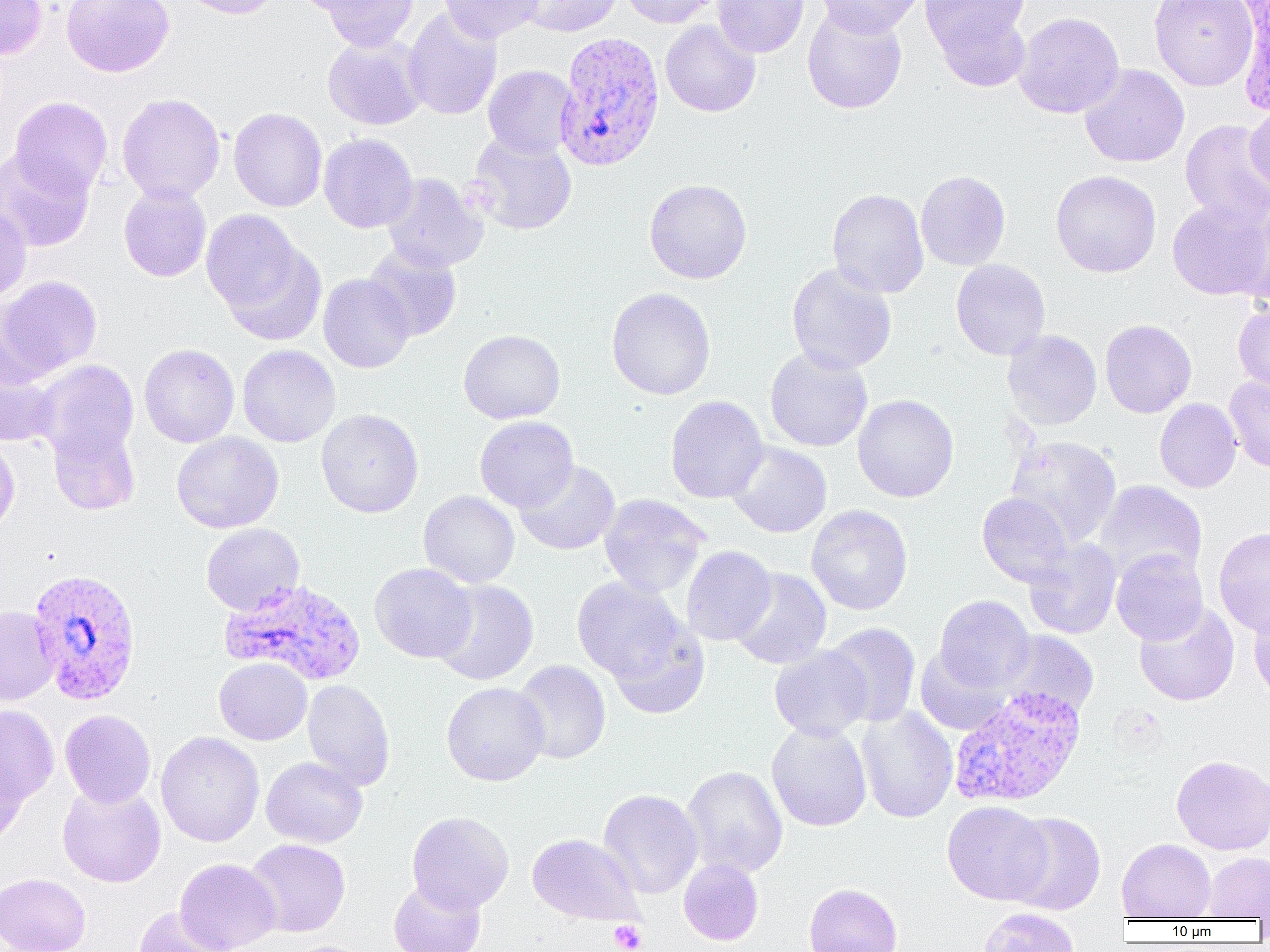

Approximate bounding boxes as (x1, y1, x2, y2) in pixels. Uninfected red blood cell locations: (0, 0, 47, 60), (60, 0, 175, 77), (177, 0, 284, 19), (287, 0, 398, 16), (316, 0, 419, 51), (438, 0, 545, 43), (515, 0, 623, 36), (620, 0, 725, 28), (713, 0, 809, 58), (815, 0, 925, 38), (921, 0, 1032, 80), (1149, 0, 1258, 91), (802, 4, 907, 114), (402, 7, 502, 121), (1013, 11, 1125, 118), (660, 20, 761, 117), (323, 34, 426, 130), (1079, 63, 1190, 168), (483, 65, 577, 159), (117, 93, 225, 204), (10, 96, 112, 199), (1245, 102, 1270, 193), (228, 107, 327, 212), (1180, 119, 1270, 227), (467, 132, 578, 235), (319, 133, 418, 233), (0, 148, 95, 252), (915, 170, 1011, 271), (1051, 170, 1162, 278), (381, 173, 488, 272), (644, 179, 752, 284), (119, 183, 211, 282), (827, 188, 929, 298), (1167, 198, 1270, 300), (0, 202, 32, 304), (1234, 202, 1270, 304), (201, 210, 308, 320), (220, 240, 327, 346), (363, 244, 462, 341), (951, 259, 1051, 360), (786, 263, 897, 374), (318, 274, 415, 373), (0, 275, 102, 380), (606, 287, 716, 400), (1233, 301, 1270, 397), (1100, 319, 1197, 418), (458, 329, 566, 424), (1002, 330, 1102, 430), (138, 344, 240, 448), (237, 345, 340, 448), (764, 346, 873, 452), (0, 354, 59, 448), (35, 359, 139, 463), (1224, 375, 1270, 473), (853, 394, 959, 502), (665, 395, 768, 503), (1155, 398, 1242, 493), (316, 408, 423, 517), (475, 416, 579, 512), (48, 421, 141, 515), (171, 431, 284, 534), (1005, 434, 1122, 548), (0, 436, 20, 539), (726, 441, 832, 538), (514, 460, 621, 556), (1094, 480, 1207, 583), (419, 491, 520, 588), (977, 492, 1074, 587), (599, 494, 710, 598), (806, 504, 913, 615), (201, 523, 305, 615), (1213, 527, 1270, 636), (1023, 539, 1123, 640), (680, 546, 777, 646), (1111, 549, 1208, 645), (369, 563, 476, 662), (730, 568, 831, 669), (572, 577, 689, 682), (431, 579, 539, 685), (934, 595, 1035, 692), (1134, 602, 1240, 706), (1248, 604, 1270, 704), (0, 606, 60, 705), (607, 621, 710, 719), (823, 623, 921, 727), (997, 630, 1099, 720), (769, 646, 872, 741), (915, 646, 1012, 736), (214, 657, 312, 745), (513, 660, 612, 765), (302, 679, 395, 791), (441, 682, 549, 785), (0, 704, 59, 807), (856, 706, 958, 824), (60, 710, 156, 807), (766, 720, 872, 832), (155, 732, 264, 847), (0, 751, 29, 853), (1171, 755, 1270, 855), (261, 756, 368, 848), (680, 765, 788, 878), (57, 782, 166, 887), (598, 788, 704, 898), (942, 801, 1052, 905), (407, 811, 513, 913), (1005, 812, 1106, 915), (527, 833, 642, 925), (1117, 838, 1216, 920), (245, 839, 350, 937), (1203, 852, 1270, 920), (175, 858, 281, 952), (678, 859, 764, 945), (1, 873, 90, 952), (388, 877, 487, 952), (803, 883, 903, 952), (132, 906, 233, 952), (979, 907, 1080, 952). White blood cell locations: (1233, 0, 1269, 116). Plasmodium vivax-infected red blood cell locations: (553, 31, 666, 172), (28, 568, 142, 705), (219, 578, 367, 686), (951, 687, 1088, 810). Platelet locations: (608, 920, 647, 952). Slide-level diagnosis: Plasmodium vivax. Thin blood smear. Captured at 1000x magnification. Light microscopy. Image is 1270×952 pixels. One field of a larger specimen.